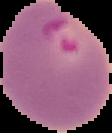

malaria status = parasitized
preparation = thin blood smear
image size = 112×133 pixels
image type = cell region segmented out of the field of view; surrounding area masked to black